Assess this cell for malaria.
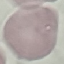
Uninfected.

Thin smear of blood. Photographed with a smartphone camera at the microscope eyepiece. Cell patch, automatically extracted from a larger field of view and resized to 64 × 64 pixels. Giemsa-stained preparation.